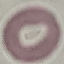 Result: negative for malaria parasites. Thin blood smear. Acquired by smartphone through the microscope eyepiece. Cell patch, automatically extracted from a larger field of view and resized to 64 × 64 pixels. Giemsa-stained preparation.